Assess this cell for malaria.
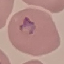
Uninfected.

Acquired by smartphone through the microscope eyepiece. Automatically extracted cell patch, resized to 64 × 64 pixels. Giemsa-stained preparation. Thin smear of blood.